Assess this cell for malaria.
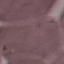

Uninfected.

Summary:
  - Capture: smartphone through the microscope eyepiece
  - Preparation: thin blood film
  - Image type: cell patch, automatically extracted from a larger field of view and resized to 64 × 64 pixels
  - Stain: Giemsa